Identify the cell.
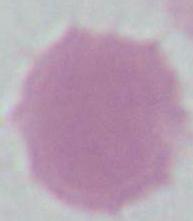
An erythrocyte.

Summary:
  - Magnification: 1000x
  - Modality: micrograph